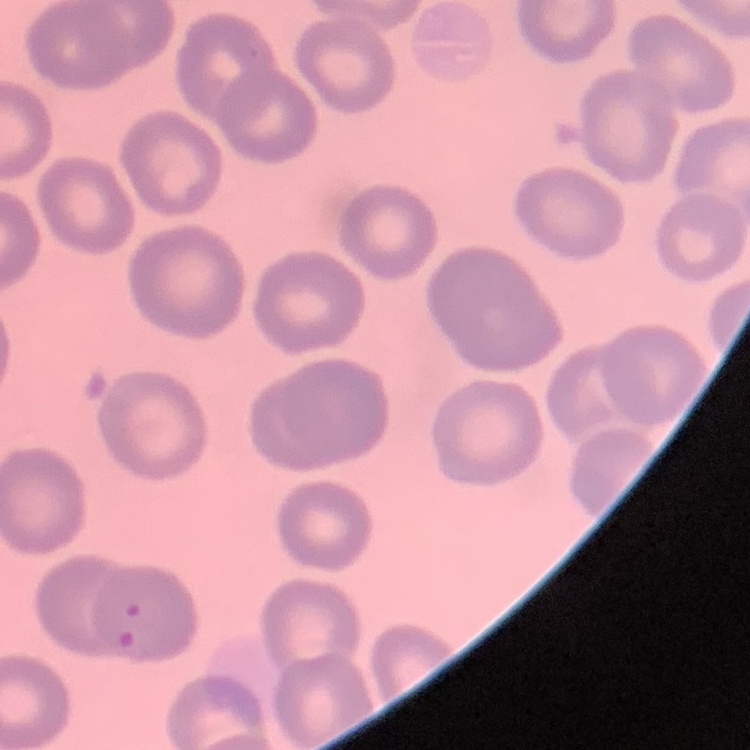

red blood cell morphology = no rouleaux formation
image type = one tile cut from a larger photomicrograph
preparation = thin blood smear
stain = Field's or Giemsa